Assess this cell for malaria.
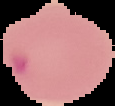

It is parasitized.

Image is 115×106 pixels. The area outside the segmented cell region is set to black. From a thin blood film.